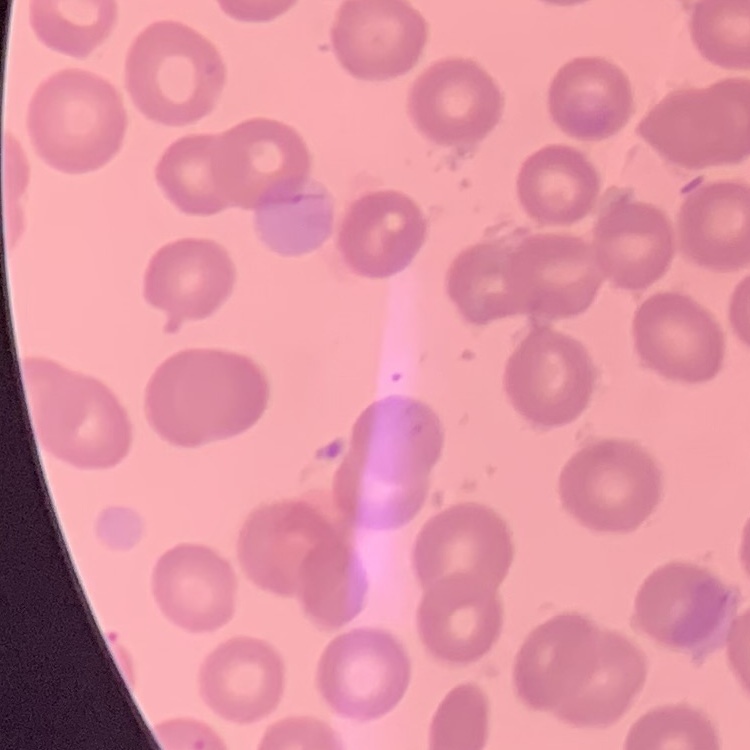
The erythrocytes exhibit no rouleaux formation. One tile cut from a larger photomicrograph. Thin blood film. Stained with either Field's or Giemsa.